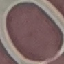 Result: no malaria parasites detected. Giemsa stain. Cell patch, automatically extracted from a larger field of view and resized to 64 × 64 pixels. Photographed with a smartphone camera at the microscope eyepiece. Thin smear of blood.